Locate every Plasmodium parasite.
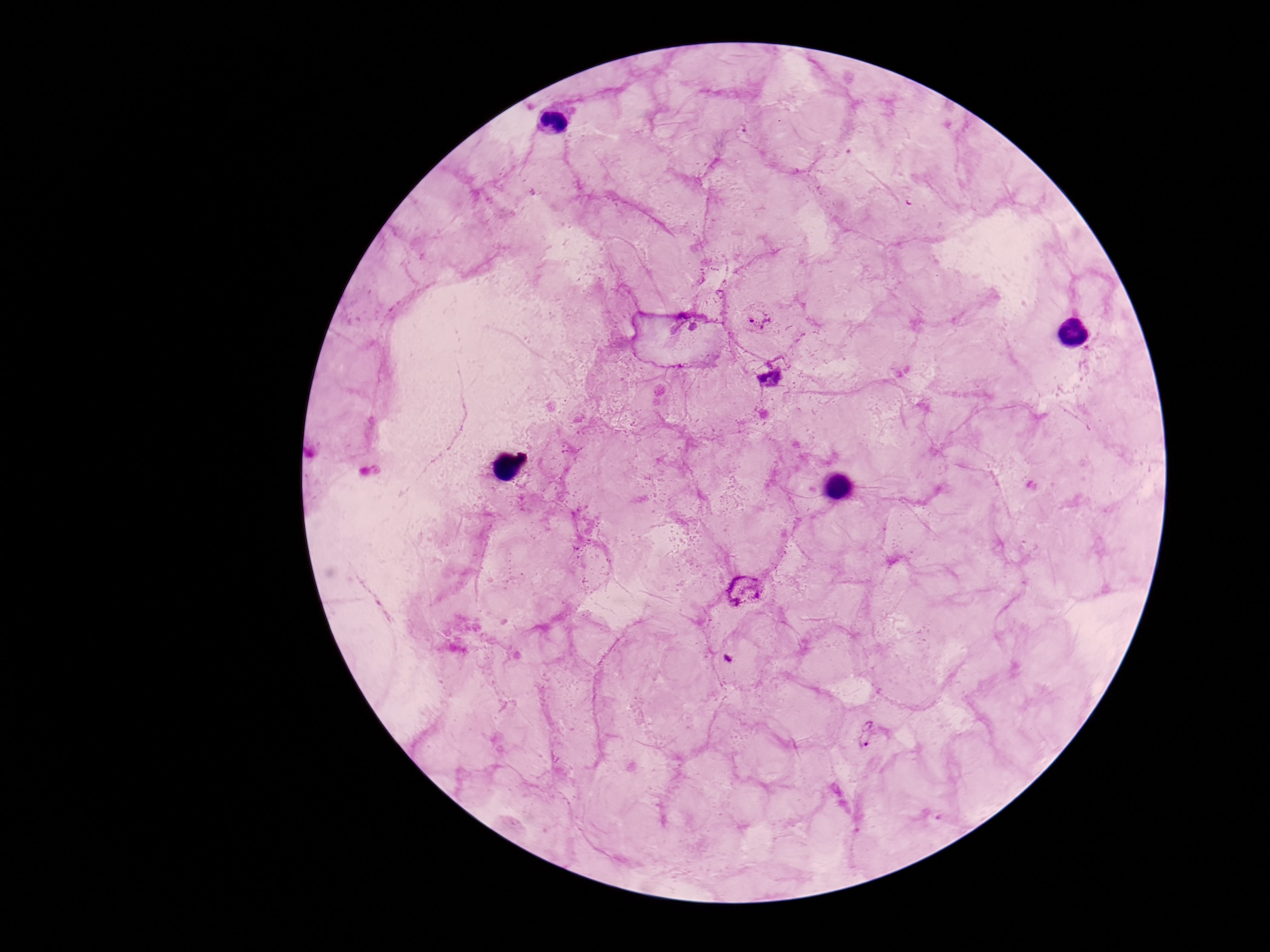
Approximate centers as [x, y] in pixels.
Plasmodium parasites: [758, 317], [770, 377], [748, 593], [867, 738].

Image is 1270×952 pixels. Patient malaria status: positive. Photographed through the microscope eyepiece with a smartphone camera. Single field of view. Thick peripheral-blood smear. 100x magnification. Giemsa stain.